Identify the cell.
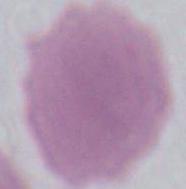

An erythrocyte.

Summary:
  - Modality: photomicrograph
  - Magnification: 1000x